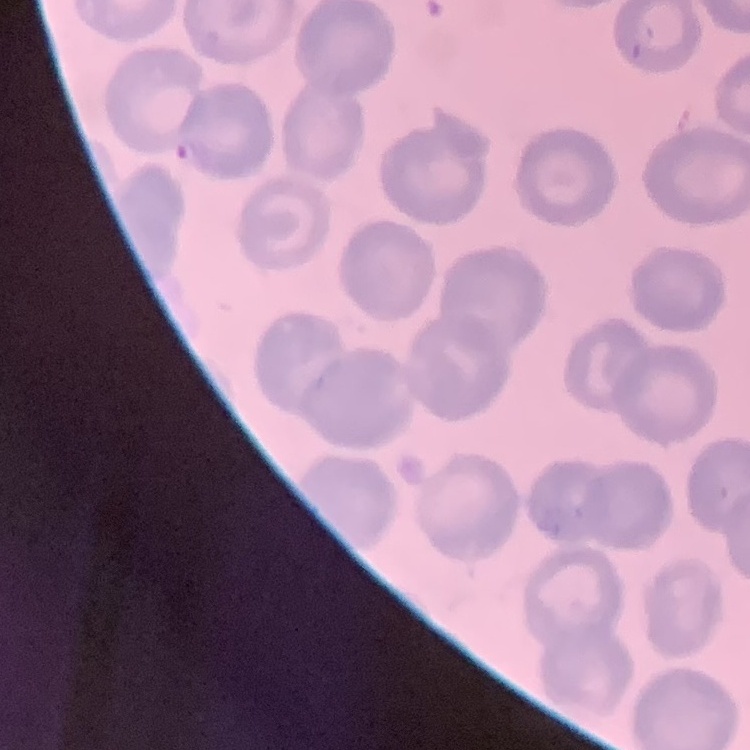
red blood cell morphology = no rouleaux formation
image type = one tile cut from a larger photomicrograph
preparation = thin blood smear
stain = Field's or Giemsa